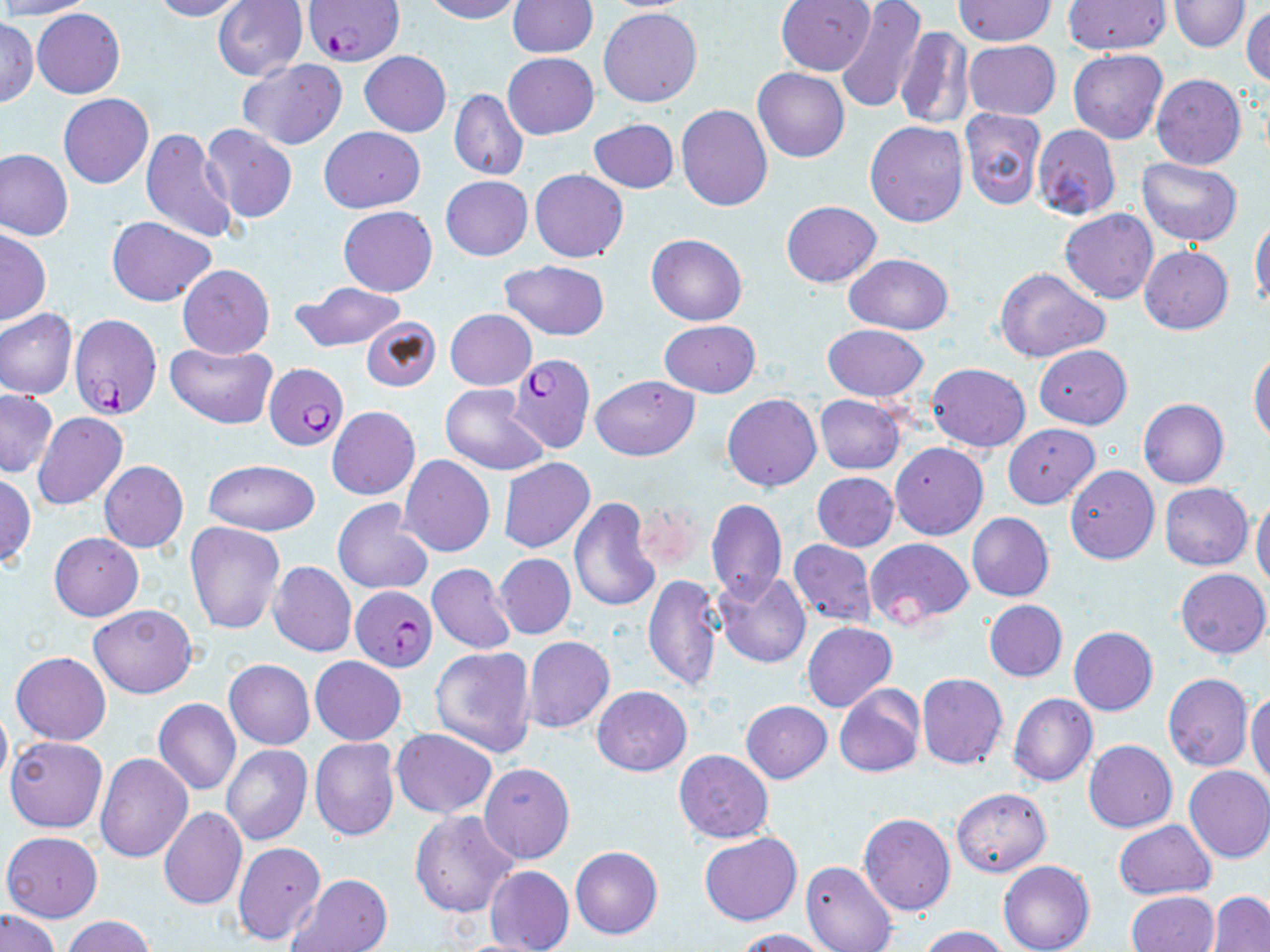

Approximate bounding boxes as named x1/y1/x2/y2 corners in pixels. Uninfected red blood cell locations: (x1=0, y1=0, x2=95, y2=19), (x1=150, y1=0, x2=247, y2=21), (x1=214, y1=0, x2=307, y2=80), (x1=422, y1=0, x2=521, y2=22), (x1=508, y1=0, x2=598, y2=57), (x1=775, y1=0, x2=874, y2=75), (x1=835, y1=0, x2=927, y2=114), (x1=1062, y1=0, x2=1171, y2=54), (x1=1168, y1=0, x2=1251, y2=52), (x1=598, y1=1, x2=701, y2=12), (x1=952, y1=1, x2=1056, y2=46), (x1=1242, y1=5, x2=1270, y2=88), (x1=32, y1=8, x2=125, y2=98), (x1=599, y1=9, x2=703, y2=108), (x1=0, y1=15, x2=37, y2=108), (x1=895, y1=28, x2=974, y2=131), (x1=964, y1=39, x2=1060, y2=120), (x1=1069, y1=49, x2=1167, y2=145), (x1=358, y1=50, x2=451, y2=136), (x1=503, y1=52, x2=599, y2=139), (x1=237, y1=58, x2=347, y2=150), (x1=753, y1=69, x2=849, y2=162), (x1=1151, y1=74, x2=1246, y2=170), (x1=448, y1=88, x2=528, y2=181), (x1=59, y1=93, x2=153, y2=189), (x1=677, y1=104, x2=772, y2=211), (x1=959, y1=108, x2=1045, y2=210), (x1=589, y1=119, x2=679, y2=193), (x1=865, y1=120, x2=968, y2=227), (x1=199, y1=124, x2=298, y2=222), (x1=1032, y1=124, x2=1120, y2=220), (x1=141, y1=125, x2=239, y2=245), (x1=319, y1=127, x2=425, y2=212), (x1=0, y1=148, x2=73, y2=241), (x1=1136, y1=157, x2=1243, y2=246), (x1=530, y1=169, x2=628, y2=262), (x1=440, y1=175, x2=532, y2=260), (x1=781, y1=201, x2=881, y2=287), (x1=337, y1=206, x2=438, y2=296), (x1=1059, y1=209, x2=1158, y2=304), (x1=107, y1=216, x2=217, y2=306), (x1=1250, y1=217, x2=1270, y2=312), (x1=0, y1=228, x2=51, y2=326), (x1=646, y1=234, x2=747, y2=325), (x1=1139, y1=247, x2=1232, y2=334), (x1=843, y1=253, x2=952, y2=334), (x1=500, y1=259, x2=610, y2=342), (x1=178, y1=264, x2=274, y2=358), (x1=994, y1=266, x2=1110, y2=362), (x1=292, y1=282, x2=407, y2=351), (x1=0, y1=308, x2=77, y2=399), (x1=446, y1=309, x2=536, y2=389), (x1=361, y1=316, x2=441, y2=392), (x1=659, y1=320, x2=760, y2=397), (x1=823, y1=325, x2=928, y2=402), (x1=166, y1=342, x2=277, y2=428), (x1=1034, y1=344, x2=1131, y2=428), (x1=1249, y1=349, x2=1270, y2=444), (x1=927, y1=363, x2=1030, y2=451), (x1=590, y1=375, x2=699, y2=460), (x1=440, y1=384, x2=550, y2=476), (x1=1, y1=389, x2=56, y2=477), (x1=722, y1=394, x2=822, y2=491), (x1=815, y1=395, x2=906, y2=474), (x1=1138, y1=398, x2=1229, y2=489), (x1=327, y1=406, x2=420, y2=500), (x1=32, y1=412, x2=128, y2=510), (x1=1003, y1=423, x2=1099, y2=509), (x1=891, y1=443, x2=987, y2=540), (x1=399, y1=455, x2=494, y2=558), (x1=498, y1=457, x2=595, y2=552), (x1=203, y1=459, x2=320, y2=536), (x1=99, y1=461, x2=188, y2=553), (x1=1066, y1=466, x2=1160, y2=564), (x1=812, y1=472, x2=898, y2=551), (x1=0, y1=473, x2=36, y2=566), (x1=1160, y1=483, x2=1253, y2=570), (x1=1251, y1=496, x2=1270, y2=589), (x1=569, y1=497, x2=660, y2=613), (x1=333, y1=498, x2=433, y2=594), (x1=706, y1=498, x2=787, y2=603), (x1=634, y1=500, x2=702, y2=575), (x1=967, y1=512, x2=1053, y2=601), (x1=185, y1=521, x2=284, y2=635), (x1=50, y1=532, x2=143, y2=620), (x1=865, y1=537, x2=973, y2=627), (x1=789, y1=540, x2=877, y2=627), (x1=496, y1=553, x2=576, y2=638), (x1=267, y1=560, x2=357, y2=656), (x1=427, y1=563, x2=517, y2=653), (x1=1176, y1=568, x2=1270, y2=660), (x1=714, y1=571, x2=811, y2=669), (x1=643, y1=574, x2=722, y2=692), (x1=984, y1=599, x2=1067, y2=681), (x1=90, y1=604, x2=196, y2=699), (x1=803, y1=622, x2=897, y2=712), (x1=1069, y1=626, x2=1158, y2=715), (x1=523, y1=636, x2=614, y2=733), (x1=430, y1=646, x2=535, y2=756), (x1=10, y1=652, x2=111, y2=745), (x1=310, y1=656, x2=406, y2=745), (x1=223, y1=658, x2=316, y2=749), (x1=917, y1=672, x2=1007, y2=770), (x1=1164, y1=674, x2=1254, y2=771), (x1=834, y1=684, x2=925, y2=780), (x1=592, y1=686, x2=692, y2=775), (x1=1247, y1=691, x2=1270, y2=786), (x1=1008, y1=693, x2=1096, y2=787), (x1=153, y1=699, x2=241, y2=796), (x1=0, y1=700, x2=11, y2=791), (x1=742, y1=700, x2=831, y2=782), (x1=391, y1=729, x2=497, y2=818), (x1=6, y1=736, x2=107, y2=833), (x1=309, y1=737, x2=400, y2=841), (x1=1084, y1=740, x2=1177, y2=833), (x1=222, y1=744, x2=312, y2=845), (x1=675, y1=750, x2=773, y2=844), (x1=95, y1=753, x2=193, y2=863), (x1=480, y1=762, x2=574, y2=864), (x1=1184, y1=765, x2=1270, y2=863), (x1=951, y1=788, x2=1052, y2=878), (x1=159, y1=807, x2=246, y2=910), (x1=410, y1=811, x2=518, y2=919), (x1=858, y1=812, x2=956, y2=915), (x1=1114, y1=820, x2=1215, y2=899), (x1=1, y1=832, x2=103, y2=923), (x1=699, y1=834, x2=803, y2=925), (x1=233, y1=841, x2=326, y2=946), (x1=571, y1=846, x2=662, y2=939), (x1=802, y1=860, x2=897, y2=952), (x1=997, y1=860, x2=1094, y2=952), (x1=484, y1=865, x2=574, y2=952), (x1=290, y1=873, x2=392, y2=952), (x1=1125, y1=891, x2=1218, y2=952), (x1=1207, y1=891, x2=1270, y2=951), (x1=0, y1=908, x2=61, y2=952), (x1=61, y1=915, x2=154, y2=952), (x1=916, y1=925, x2=1011, y2=952), (x1=736, y1=928, x2=834, y2=951), (x1=446, y1=937, x2=552, y2=952). Plasmodium falciparum-infected red blood cell locations: (x1=308, y1=0, x2=405, y2=67), (x1=68, y1=313, x2=161, y2=422), (x1=506, y1=354, x2=594, y2=453), (x1=265, y1=363, x2=348, y2=451), (x1=350, y1=584, x2=436, y2=670). Slide-level diagnosis: Plasmodium falciparum. 1000x magnification. One field of a larger specimen. Thin blood film. May-Grünwald-Giemsa-stained preparation. Light microscopy. Image is 1270×952 pixels.